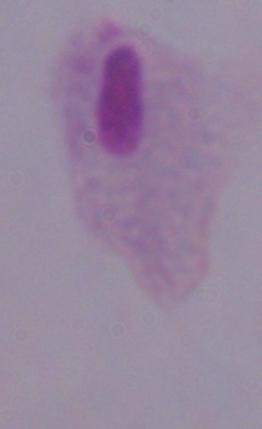

magnification = 1000x
identification = trichomonad
modality = photomicrograph